Outline each Plasmodium malariae-infected red blood cell.
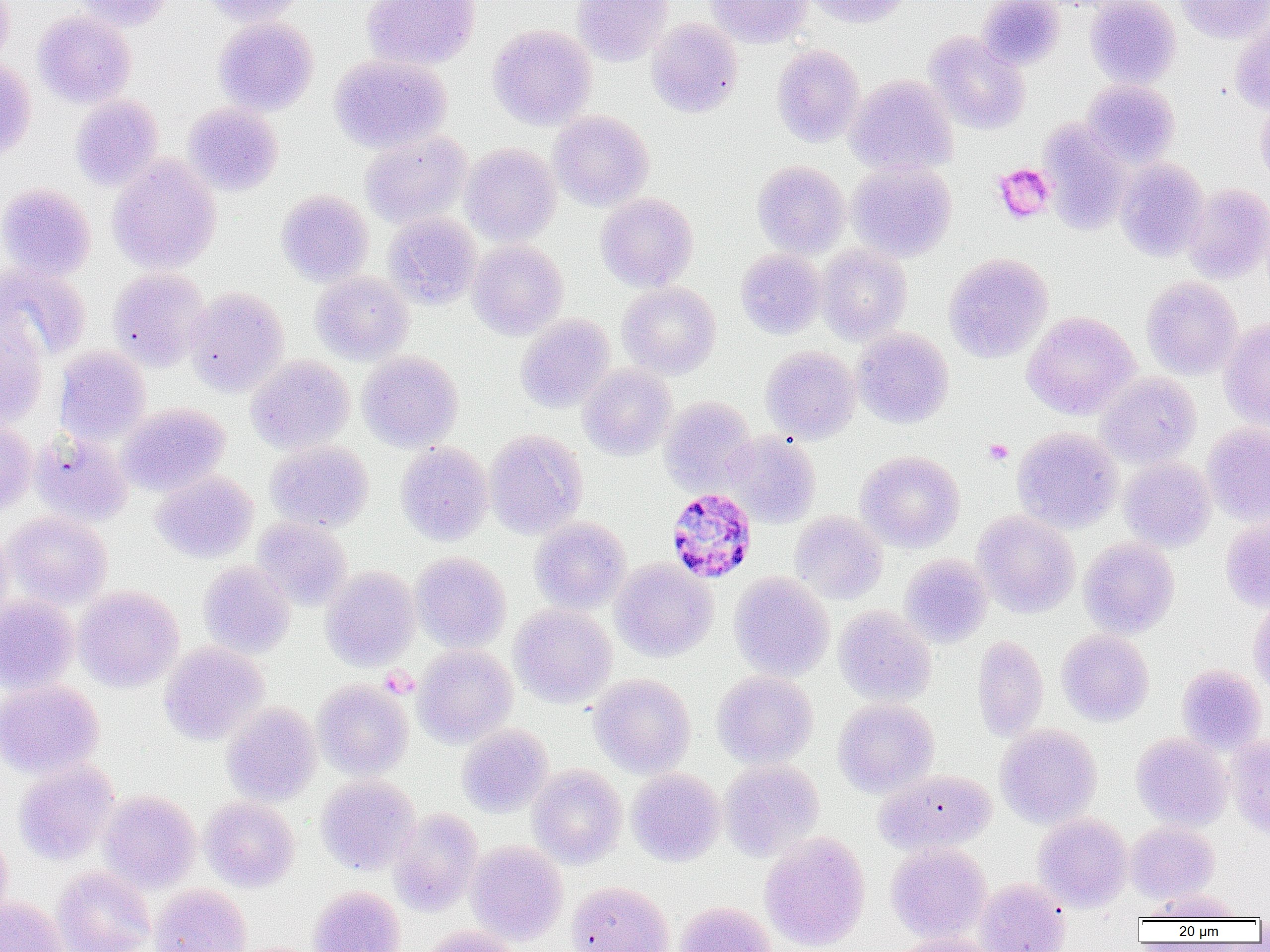

Approximate bounding boxes as [x1, y1, x2, y2] in pixels.
Plasmodium malariae-infected red blood cells: [665, 488, 757, 584].

slide-level diagnosis = Plasmodium malariae
magnification = 1000x
image size = 1270×952 pixels
field of view = one of a larger specimen
modality = optical microscopy
preparation = thin blood smear
platelet locations = approximate bounding boxes as [x1, y1, x2, y2] in pixels: [993, 163, 1055, 223], [984, 439, 1013, 465], [380, 666, 417, 699]
uninfected red blood cell locations = approximate bounding boxes as [x1, y1, x2, y2] in pixels: [72, 0, 175, 31], [200, 0, 304, 26], [361, 0, 481, 70], [572, 0, 673, 66], [705, 0, 811, 48], [803, 0, 913, 27], [977, 0, 1065, 70], [1085, 0, 1181, 89], [1175, 0, 1270, 43], [0, 1, 13, 66], [33, 11, 137, 107], [213, 17, 318, 116], [646, 18, 743, 118], [1231, 18, 1270, 113], [488, 24, 597, 130], [924, 32, 1030, 134], [771, 44, 865, 147], [329, 53, 451, 153], [0, 57, 35, 160], [846, 74, 957, 177], [1082, 79, 1180, 168], [70, 94, 164, 191], [1255, 96, 1270, 190], [182, 102, 283, 196], [548, 111, 653, 211], [1039, 120, 1133, 235], [360, 131, 471, 228], [460, 142, 561, 246], [107, 154, 222, 274], [1115, 158, 1210, 261], [752, 160, 850, 258], [847, 162, 956, 262], [0, 182, 96, 281], [1184, 184, 1270, 283], [276, 189, 374, 286], [596, 193, 698, 291], [383, 212, 483, 309], [467, 240, 568, 339], [816, 244, 912, 344], [736, 248, 826, 339], [943, 252, 1053, 362], [0, 262, 92, 362], [107, 267, 211, 371], [311, 271, 414, 365], [1142, 276, 1243, 379], [617, 281, 721, 379], [185, 287, 289, 396], [1022, 311, 1140, 419], [515, 314, 615, 413], [0, 317, 49, 428], [1219, 319, 1270, 431], [852, 327, 954, 428], [54, 346, 151, 446], [761, 346, 860, 444], [357, 351, 462, 451], [246, 354, 355, 454], [578, 364, 676, 461], [1096, 372, 1201, 468], [659, 396, 758, 495], [117, 403, 231, 496], [0, 422, 37, 515], [1202, 423, 1270, 524], [1012, 427, 1123, 533], [484, 429, 587, 539], [29, 431, 133, 525], [725, 431, 821, 528], [266, 440, 374, 532], [395, 441, 493, 546], [856, 451, 965, 552], [1119, 457, 1216, 552], [150, 470, 258, 563], [3, 511, 112, 608], [790, 511, 887, 604], [973, 511, 1080, 617], [1220, 515, 1270, 613], [253, 517, 352, 610], [530, 517, 631, 613], [0, 527, 14, 625], [1078, 537, 1180, 638], [410, 551, 511, 653], [900, 553, 993, 647], [610, 558, 718, 662], [198, 560, 295, 658], [321, 566, 421, 671], [729, 572, 834, 681], [73, 585, 184, 692], [0, 594, 79, 694], [1248, 597, 1270, 701], [509, 604, 616, 708], [834, 605, 936, 706], [1057, 629, 1154, 725], [972, 635, 1048, 741], [159, 641, 269, 745], [413, 644, 517, 747], [1176, 664, 1266, 754], [712, 670, 818, 768], [588, 674, 696, 778], [0, 679, 104, 779], [313, 679, 413, 780], [833, 698, 939, 797], [222, 702, 321, 806], [457, 724, 553, 817], [995, 724, 1102, 829], [1131, 732, 1232, 830], [1226, 733, 1270, 838], [719, 759, 824, 861], [13, 760, 120, 865], [527, 764, 627, 868], [626, 768, 725, 866], [873, 768, 996, 855], [315, 774, 420, 875], [98, 790, 201, 893], [200, 797, 300, 892], [388, 807, 484, 915], [1033, 812, 1133, 911], [1126, 822, 1220, 903], [0, 829, 13, 926], [759, 832, 871, 951], [466, 840, 568, 944], [886, 842, 992, 943], [52, 865, 155, 952], [975, 878, 1071, 952], [566, 880, 675, 952], [149, 884, 252, 952], [308, 886, 406, 952], [1146, 888, 1243, 921], [0, 896, 68, 952], [674, 901, 777, 952], [417, 926, 522, 952], [889, 934, 999, 952]